Outline each Plasmodium falciparum parasite and classify it by life-cycle stage.
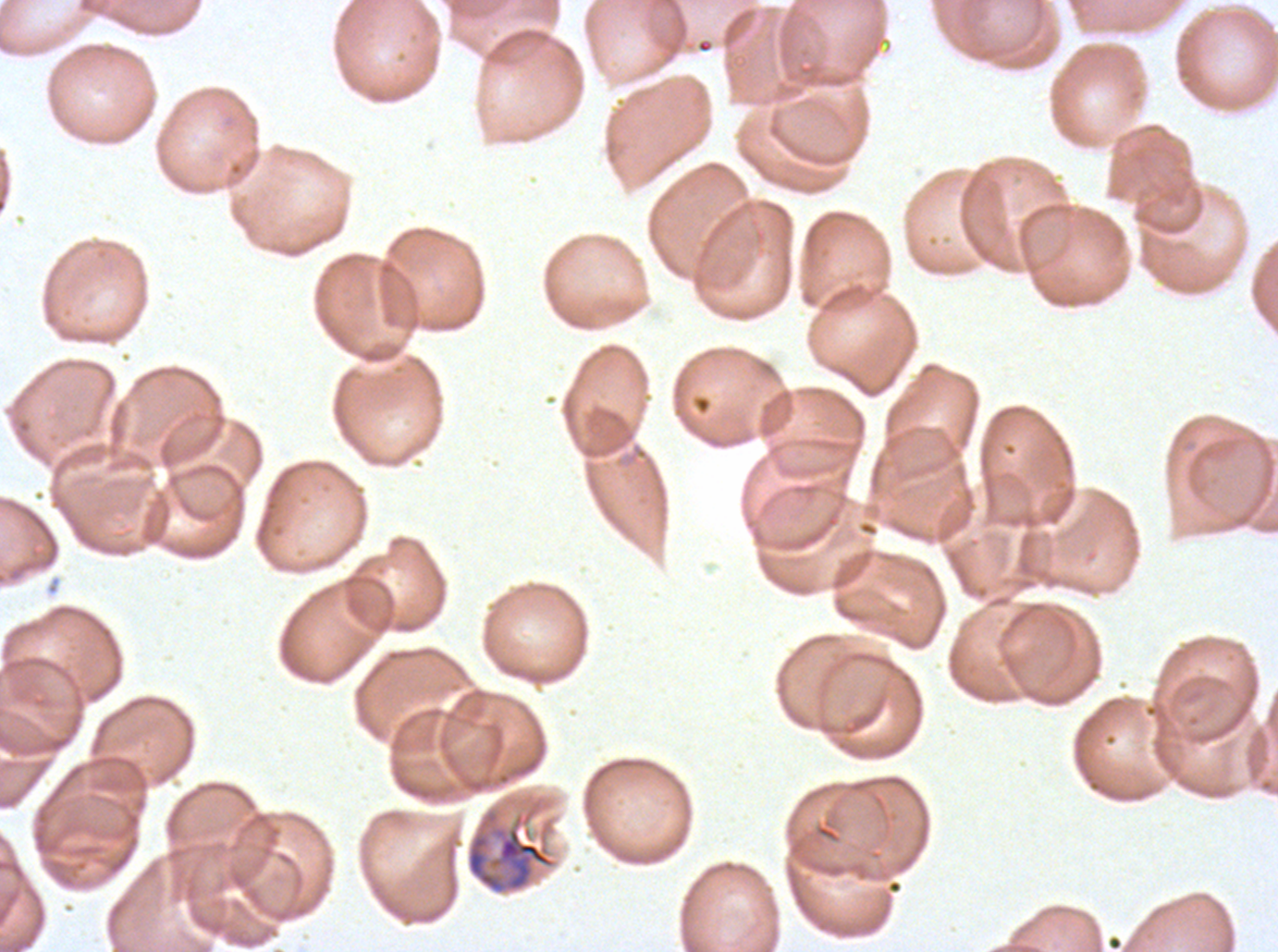

Approximate bounding boxes as [x1, y1, x2, y2] in pixels.
Late trophozoites: [465, 807, 557, 895].
No rings, late-ring/early-trophozoite forms, mid trophozoites, early schizonts, late schizonts, segmenters, or gametocytes observed.

stain: Giemsa
image_size: 1278×952 pixels
preparation: thin blood smear
field_of_view: one sub-image of a larger composite
specimen: Plasmodium falciparum from a patient in The Gambia, cultured ex vivo for 24 to 48 hours